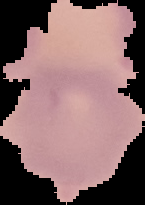
image_size: 145×205 pixels
result: no Plasmodium parasites detected
image_type: segmented cell region on a black background
preparation: thin blood smear